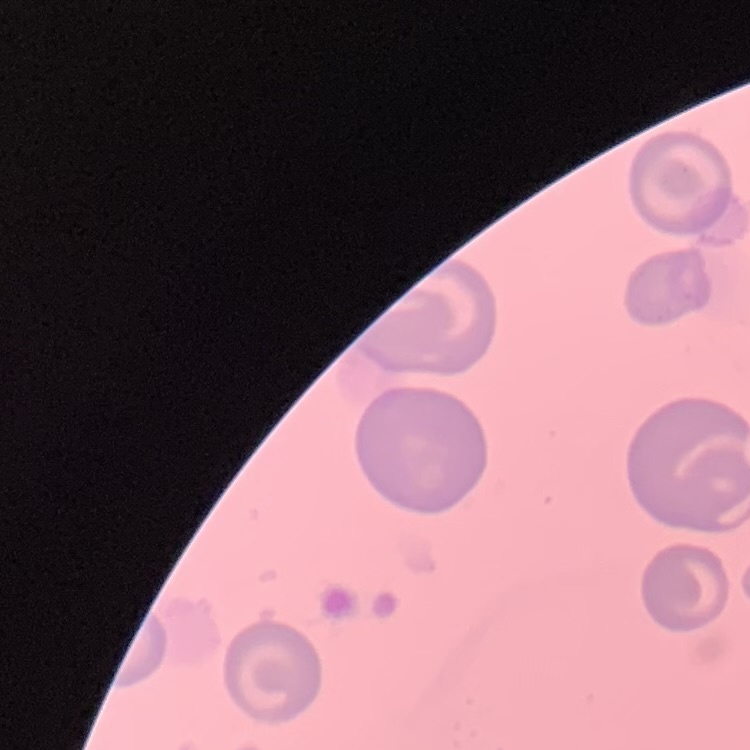

The erythrocytes show no rouleaux formation. Square crop of a larger photomicrograph. Stained with either Field's or Giemsa. Thin peripheral smear.